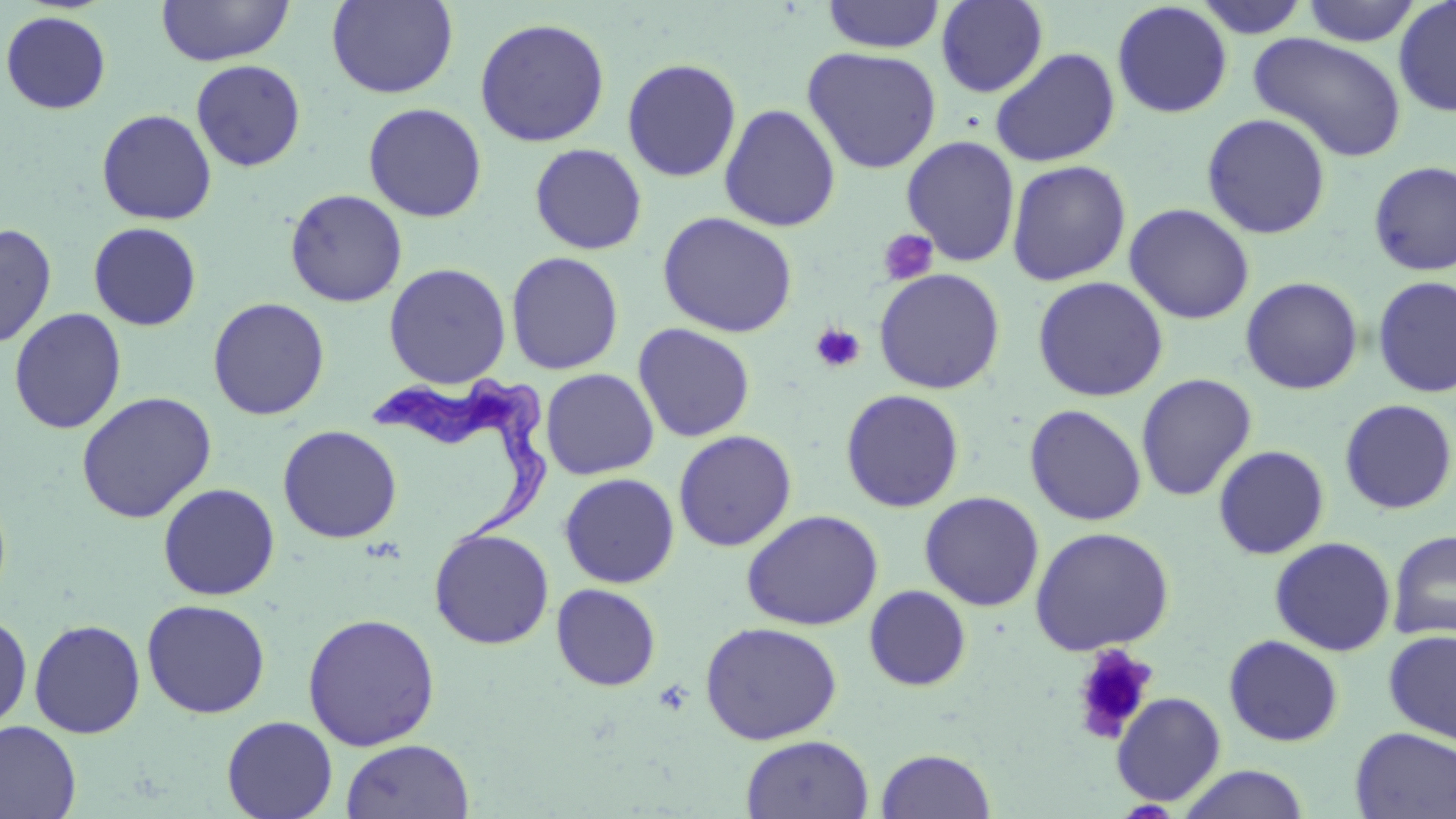

Summary:
  - Coordinate format: approximate bounding boxes as (x1,y1)-(x2,y2) corner pairs in pixels
  - Platelet locations: (878,229)-(939,286), (810,323)-(866,373)
  - Trypanosoma brucei locations: (372,366)-(558,554)
  - Uninfected red blood cell locations: (156,0)-(294,66), (326,0)-(458,99), (1192,0)-(1313,38), (1300,0)-(1423,46), (1393,0)-(1456,117), (820,1)-(946,53), (935,1)-(1048,97), (1111,1)-(1233,118), (1,10)-(112,114), (474,17)-(611,147), (1248,32)-(1407,162), (802,46)-(942,174), (990,47)-(1120,167), (621,58)-(742,182), (191,60)-(306,171), (363,102)-(487,223), (719,104)-(841,232), (96,109)-(217,225), (1201,112)-(1332,240), (900,135)-(1020,267), (529,143)-(648,255), (1006,159)-(1132,286), (1369,160)-(1456,276), (285,188)-(408,307), (1124,203)-(1255,325), (657,211)-(799,338), (88,222)-(202,331), (0,223)-(57,348), (505,251)-(624,375), (383,263)-(512,389), (873,268)-(1006,394), (1372,275)-(1456,398), (1032,276)-(1169,402), (1240,276)-(1363,395), (207,297)-(330,420), (8,308)-(127,434), (633,323)-(755,442), (540,368)-(659,480), (1135,373)-(1257,502), (840,389)-(965,512), (76,391)-(217,523), (1339,399)-(1455,515), (1024,404)-(1147,526), (278,425)-(402,544), (673,430)-(797,551), (1213,445)-(1330,559), (559,472)-(680,588), (157,482)-(280,600), (919,491)-(1044,612), (740,509)-(884,631), (1029,526)-(1175,655), (429,527)-(555,650), (1388,528)-(1455,642), (1269,537)-(1396,656), (551,583)-(661,691), (864,585)-(971,692), (141,598)-(271,719), (0,610)-(33,734), (302,612)-(441,751), (29,618)-(146,739), (699,621)-(842,745), (1383,629)-(1456,745), (1223,635)-(1344,747), (1069,641)-(1159,745), (1111,691)-(1226,806), (221,715)-(338,819), (0,720)-(81,819), (1350,727)-(1456,818), (741,734)-(874,819), (341,738)-(474,819), (875,748)-(996,819), (1176,765)-(1311,819)
  - Slide-level diagnosis: Trypanosoma brucei
  - Stain: May-Grünwald-Giemsa
  - Field of view: single
  - Modality: optical microscopy
  - Magnification: 1000x
  - Preparation: thin blood film
  - Image size: 1456×819 pixels